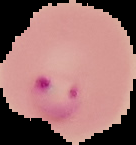

Image is 136×145 pixels. From a thin blood smear. Result: malaria parasites detected. Segmented cell region on a black background.